Outline each blood parasite and name the species.
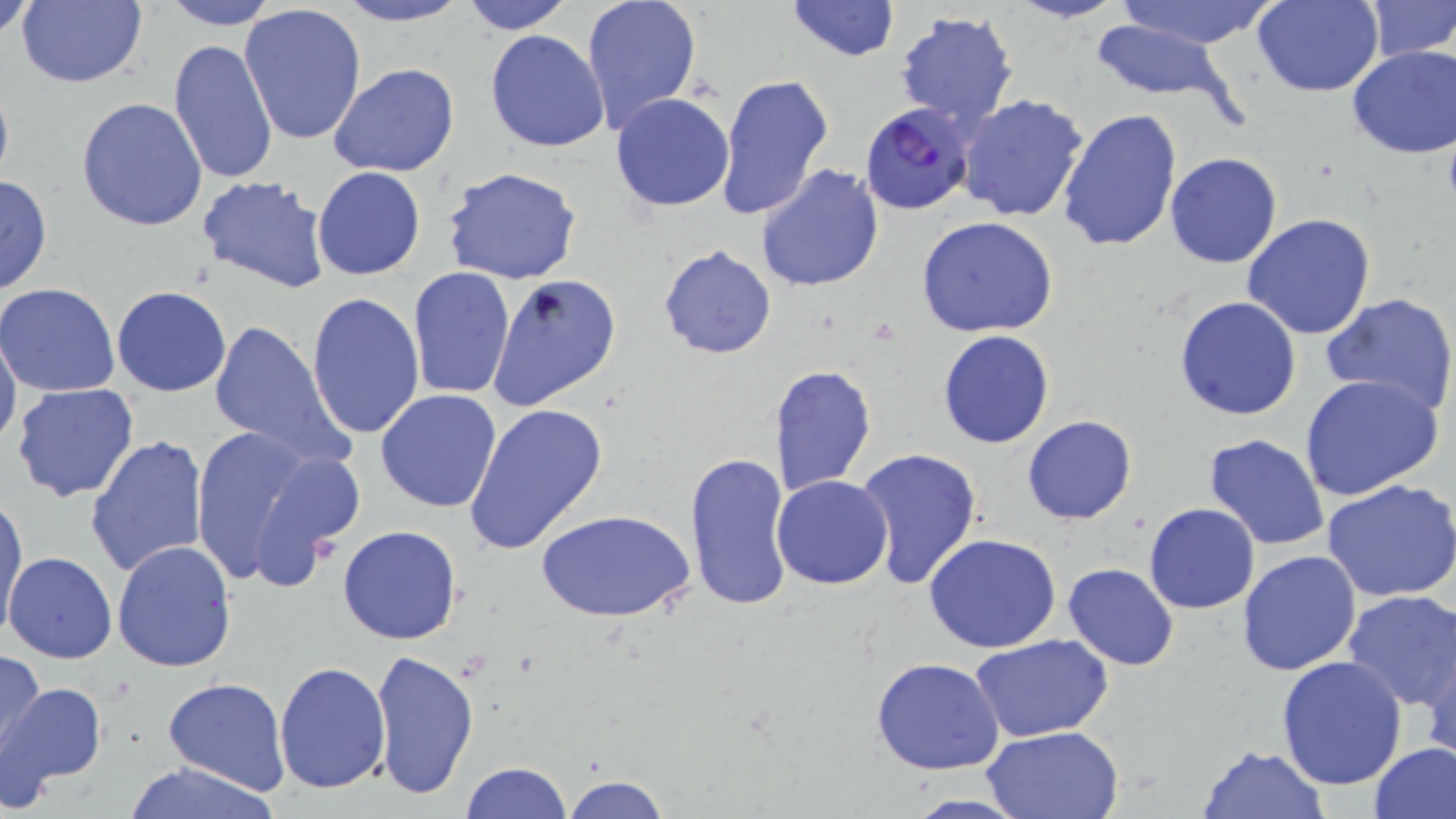

Approximate bounding boxes as (x1, y1, x2, y2) in pixels.
Plasmodium falciparum-infected red blood cells: (863, 103, 976, 216).
No Plasmodium ovale, Plasmodium malariae, Plasmodium vivax, Babesia divergens, or Trypanosoma brucei observed.

Summary:
  - Uninfected red blood cell locations: (1, 0, 41, 42), (16, 0, 148, 88), (334, 0, 470, 27), (459, 0, 574, 34), (580, 0, 703, 135), (783, 0, 901, 64), (1009, 0, 1127, 24), (1112, 0, 1281, 49), (1251, 0, 1383, 96), (1363, 0, 1456, 61), (159, 1, 280, 30), (239, 4, 367, 146), (894, 11, 1019, 130), (1087, 19, 1241, 107), (484, 29, 610, 152), (169, 38, 279, 187), (1347, 45, 1456, 159), (328, 64, 459, 179), (714, 72, 835, 220), (611, 94, 735, 212), (955, 94, 1089, 223), (75, 97, 208, 231), (1058, 107, 1183, 254), (1164, 151, 1283, 269), (755, 164, 884, 293), (442, 165, 581, 285), (312, 167, 426, 280), (195, 174, 332, 294), (0, 175, 53, 298), (1241, 213, 1376, 341), (917, 217, 1061, 337), (659, 244, 777, 360), (408, 266, 515, 400), (491, 275, 623, 410), (1, 283, 120, 397), (112, 286, 232, 397), (307, 291, 425, 440), (1322, 292, 1456, 421), (1174, 296, 1303, 421), (207, 318, 348, 470), (0, 327, 22, 454), (938, 330, 1054, 448), (767, 364, 877, 498), (1299, 373, 1445, 499), (9, 382, 139, 503), (375, 389, 503, 512), (463, 403, 608, 554), (1022, 415, 1137, 524), (186, 425, 360, 593), (85, 435, 209, 581), (1202, 435, 1331, 551), (854, 447, 983, 588), (686, 449, 794, 611), (772, 475, 893, 589), (1321, 479, 1456, 604), (1, 490, 28, 642), (1144, 503, 1259, 614), (537, 508, 696, 625), (337, 526, 462, 646), (922, 534, 1064, 655), (112, 539, 238, 671), (1237, 551, 1364, 676), (5, 552, 118, 663), (1063, 562, 1179, 670), (1340, 590, 1456, 712), (971, 634, 1113, 742), (1420, 638, 1455, 767), (0, 645, 45, 762), (370, 648, 479, 801), (871, 656, 1006, 774), (1276, 657, 1408, 791), (274, 661, 391, 794), (163, 676, 291, 793), (0, 681, 106, 804), (980, 726, 1124, 819), (1370, 741, 1456, 819), (1196, 744, 1331, 818), (122, 760, 281, 819), (459, 761, 572, 818), (560, 775, 671, 819), (896, 793, 1031, 818)
  - Slide-level diagnosis: Plasmodium falciparum
  - Magnification: 1000x
  - Field of view: single
  - Image size: 1456×819 pixels
  - Modality: light microscopy
  - Preparation: thin blood smear
  - Stain: May-Grünwald-Giemsa